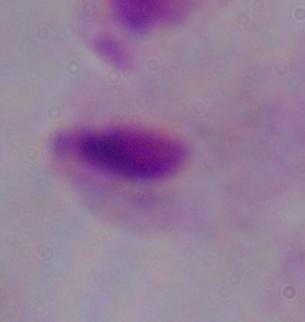

Summary:
  - Identification: trichomonad
  - Magnification: 1000x
  - Modality: photomicrograph